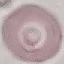
{
  "result": "no malaria parasites detected",
  "stain": "Giemsa",
  "capture": "smartphone camera at the microscope eyepiece",
  "preparation": "thin smear",
  "image_type": "cell patch, automatically extracted from a larger field of view and resized to 64 × 64 pixels"
}